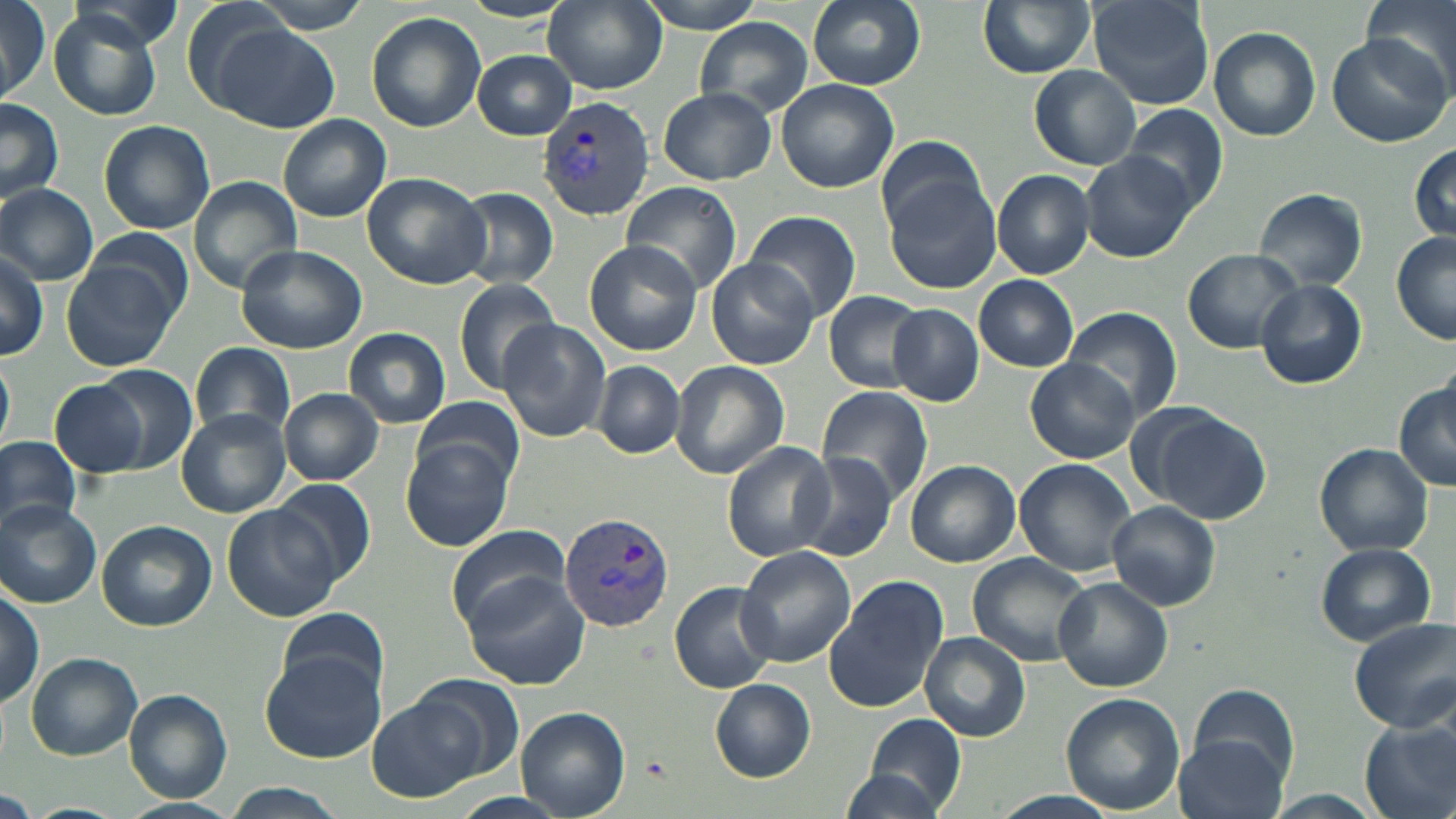

Approximate bounding boxes as named x1/y1/x2/y2 corners in pixels. Plasmodium vivax-infected red blood cell locations: (x1=541, y1=96, x2=655, y2=220), (x1=558, y1=509, x2=677, y2=633). Uninfected red blood cell locations: (x1=0, y1=0, x2=53, y2=104), (x1=54, y1=0, x2=188, y2=49), (x1=245, y1=0, x2=375, y2=33), (x1=543, y1=0, x2=667, y2=93), (x1=637, y1=0, x2=770, y2=34), (x1=807, y1=0, x2=926, y2=89), (x1=977, y1=0, x2=1094, y2=79), (x1=1090, y1=0, x2=1214, y2=109), (x1=1362, y1=0, x2=1455, y2=82), (x1=45, y1=9, x2=164, y2=121), (x1=366, y1=11, x2=487, y2=132), (x1=695, y1=17, x2=814, y2=118), (x1=212, y1=25, x2=338, y2=133), (x1=1209, y1=27, x2=1320, y2=141), (x1=1327, y1=30, x2=1454, y2=148), (x1=472, y1=50, x2=576, y2=138), (x1=1028, y1=66, x2=1139, y2=169), (x1=776, y1=78, x2=899, y2=192), (x1=658, y1=89, x2=776, y2=184), (x1=0, y1=98, x2=65, y2=204), (x1=1123, y1=105, x2=1231, y2=213), (x1=278, y1=115, x2=392, y2=221), (x1=97, y1=120, x2=215, y2=235), (x1=876, y1=134, x2=989, y2=237), (x1=1409, y1=145, x2=1455, y2=244), (x1=1082, y1=149, x2=1195, y2=263), (x1=991, y1=169, x2=1095, y2=278), (x1=362, y1=172, x2=493, y2=289), (x1=190, y1=177, x2=301, y2=292), (x1=884, y1=177, x2=1002, y2=295), (x1=0, y1=183, x2=99, y2=285), (x1=621, y1=184, x2=742, y2=292), (x1=454, y1=187, x2=559, y2=290), (x1=1253, y1=187, x2=1370, y2=291), (x1=743, y1=210, x2=863, y2=322), (x1=84, y1=227, x2=194, y2=322), (x1=1391, y1=232, x2=1456, y2=345), (x1=584, y1=240, x2=703, y2=354), (x1=235, y1=244, x2=367, y2=353), (x1=0, y1=247, x2=48, y2=360), (x1=1182, y1=249, x2=1305, y2=353), (x1=707, y1=257, x2=816, y2=370), (x1=62, y1=259, x2=177, y2=371), (x1=973, y1=275, x2=1079, y2=371), (x1=452, y1=278, x2=560, y2=395), (x1=1254, y1=279, x2=1368, y2=389), (x1=692, y1=290, x2=807, y2=461), (x1=824, y1=290, x2=928, y2=392), (x1=886, y1=303, x2=984, y2=407), (x1=1064, y1=305, x2=1183, y2=425), (x1=498, y1=321, x2=611, y2=443), (x1=344, y1=329, x2=451, y2=428), (x1=190, y1=342, x2=296, y2=441), (x1=0, y1=354, x2=15, y2=452), (x1=1025, y1=359, x2=1138, y2=463), (x1=668, y1=360, x2=790, y2=478), (x1=593, y1=361, x2=684, y2=458), (x1=84, y1=363, x2=199, y2=473), (x1=49, y1=375, x2=159, y2=481), (x1=1394, y1=380, x2=1456, y2=490), (x1=814, y1=386, x2=938, y2=507), (x1=279, y1=388, x2=383, y2=486), (x1=413, y1=396, x2=524, y2=490), (x1=1141, y1=407, x2=1272, y2=525), (x1=176, y1=409, x2=290, y2=518), (x1=0, y1=436, x2=81, y2=534), (x1=401, y1=438, x2=514, y2=552), (x1=722, y1=442, x2=838, y2=561), (x1=1314, y1=442, x2=1433, y2=556), (x1=795, y1=451, x2=899, y2=562), (x1=904, y1=459, x2=1022, y2=567), (x1=1014, y1=460, x2=1138, y2=575), (x1=270, y1=477, x2=377, y2=587), (x1=0, y1=500, x2=101, y2=608), (x1=1107, y1=501, x2=1222, y2=609), (x1=224, y1=504, x2=339, y2=623), (x1=97, y1=521, x2=218, y2=632), (x1=445, y1=523, x2=572, y2=630), (x1=1315, y1=541, x2=1436, y2=646), (x1=734, y1=545, x2=856, y2=666), (x1=966, y1=553, x2=1093, y2=667), (x1=463, y1=573, x2=589, y2=691), (x1=824, y1=573, x2=949, y2=714), (x1=1053, y1=577, x2=1174, y2=692), (x1=669, y1=581, x2=779, y2=694), (x1=0, y1=589, x2=46, y2=707), (x1=276, y1=605, x2=388, y2=704), (x1=1350, y1=617, x2=1456, y2=734), (x1=920, y1=633, x2=1029, y2=741), (x1=262, y1=651, x2=384, y2=764), (x1=25, y1=652, x2=142, y2=760), (x1=409, y1=676, x2=525, y2=784), (x1=710, y1=679, x2=814, y2=780), (x1=1188, y1=684, x2=1298, y2=784), (x1=124, y1=689, x2=233, y2=803), (x1=368, y1=693, x2=487, y2=803), (x1=1058, y1=693, x2=1185, y2=814), (x1=516, y1=707, x2=630, y2=817), (x1=862, y1=712, x2=968, y2=814), (x1=1359, y1=717, x2=1455, y2=819), (x1=1174, y1=733, x2=1288, y2=819), (x1=841, y1=767, x2=947, y2=819), (x1=224, y1=784, x2=344, y2=819), (x1=0, y1=788, x2=41, y2=818), (x1=987, y1=790, x2=1123, y2=819), (x1=1251, y1=790, x2=1395, y2=819), (x1=448, y1=793, x2=568, y2=819). Slide-level diagnosis: Plasmodium vivax. Thin blood film. 1000x magnification. Optical microscopy. May-Grünwald-Giemsa stain. One field of a larger specimen. Image is 1456×819 pixels.